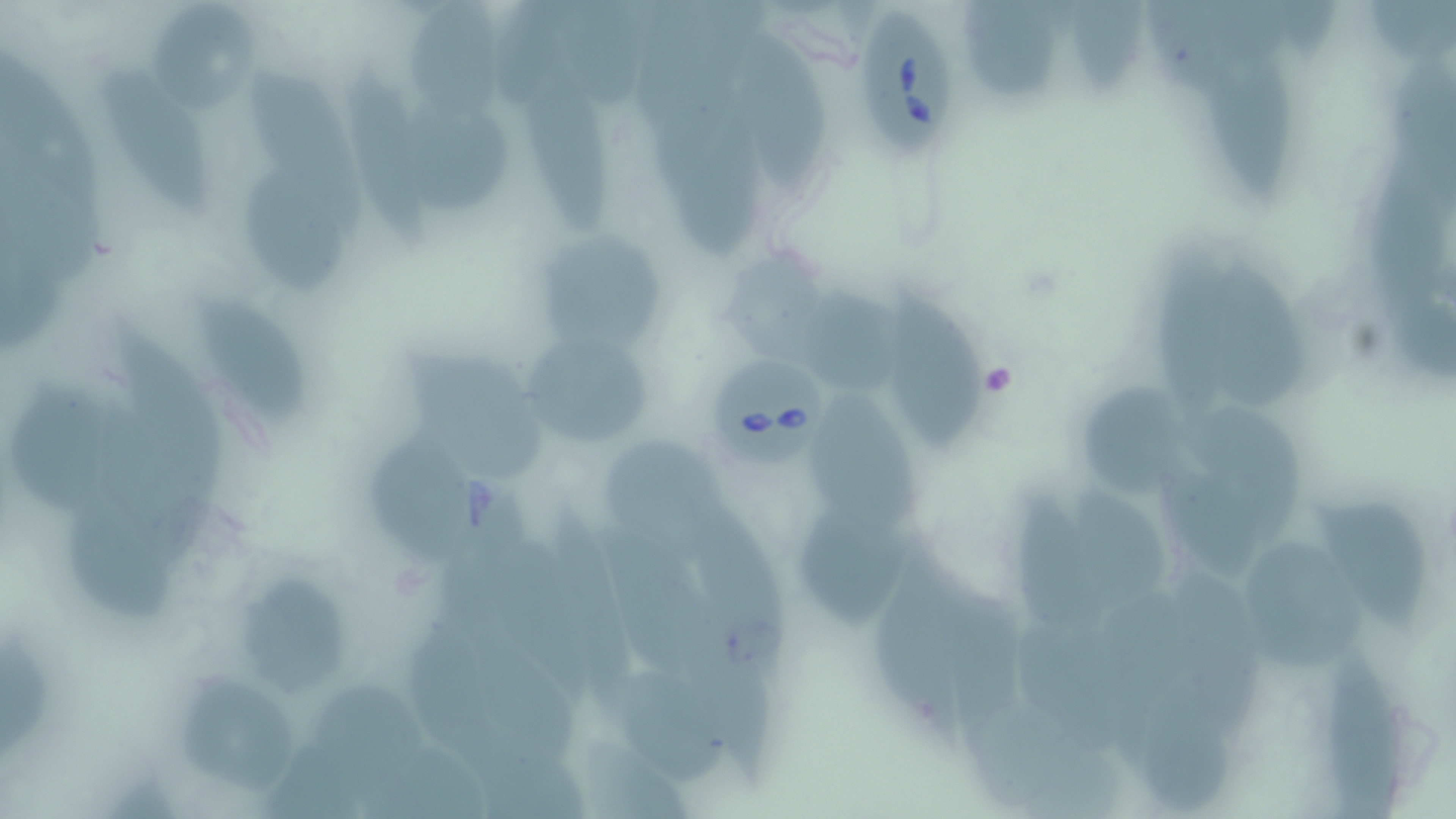
{
  "slide_level_diagnosis": "Babesia divergens",
  "preparation": "thin blood smear",
  "stain": "May-Grünwald-Giemsa",
  "modality": "optical microscopy",
  "field_of_view": "single",
  "uninfected_red_blood_cell_locations": "approximate bounding boxes as (x1,y1)-(x2,y2) corner pairs in pixels: (409,1)-(507,125), (151,3)-(263,105), (969,3)-(1060,104), (736,28)-(831,194), (1208,47)-(1303,208), (523,57)-(615,241), (348,58)-(441,248), (254,70)-(363,214), (105,75)-(220,223), (411,96)-(515,216), (679,105)-(771,263), (252,173)-(348,290), (541,234)-(670,355), (1208,249)-(1309,416), (891,286)-(985,456), (804,292)-(918,393), (195,298)-(311,422), (529,343)-(652,445), (408,352)-(554,488), (1068,377)-(1197,505), (9,381)-(119,514), (813,394)-(927,543), (1181,396)-(1307,533), (373,423)-(477,563), (606,437)-(726,569), (1167,473)-(1272,584), (1073,482)-(1173,612), (1022,489)-(1117,632), (1313,496)-(1433,636), (692,501)-(798,680), (71,505)-(177,620), (801,515)-(913,627), (490,535)-(597,708), (1250,542)-(1369,669), (874,562)-(965,743), (1162,564)-(1272,720), (243,577)-(351,696), (1330,653)-(1408,819), (618,671)-(733,789), (1141,673)-(1234,813), (188,683)-(295,796), (315,687)-(434,811), (975,698)-(1128,816)",
  "babesia_divergens_infected_red_blood_cell_locations": "approximate bounding boxes as (x1,y1)-(x2,y2) corner pairs in pixels: (851,8)-(954,156), (710,354)-(829,464)",
  "image_size": "1456×819 pixels",
  "magnification": "1000x"
}